State the blood parasite species.
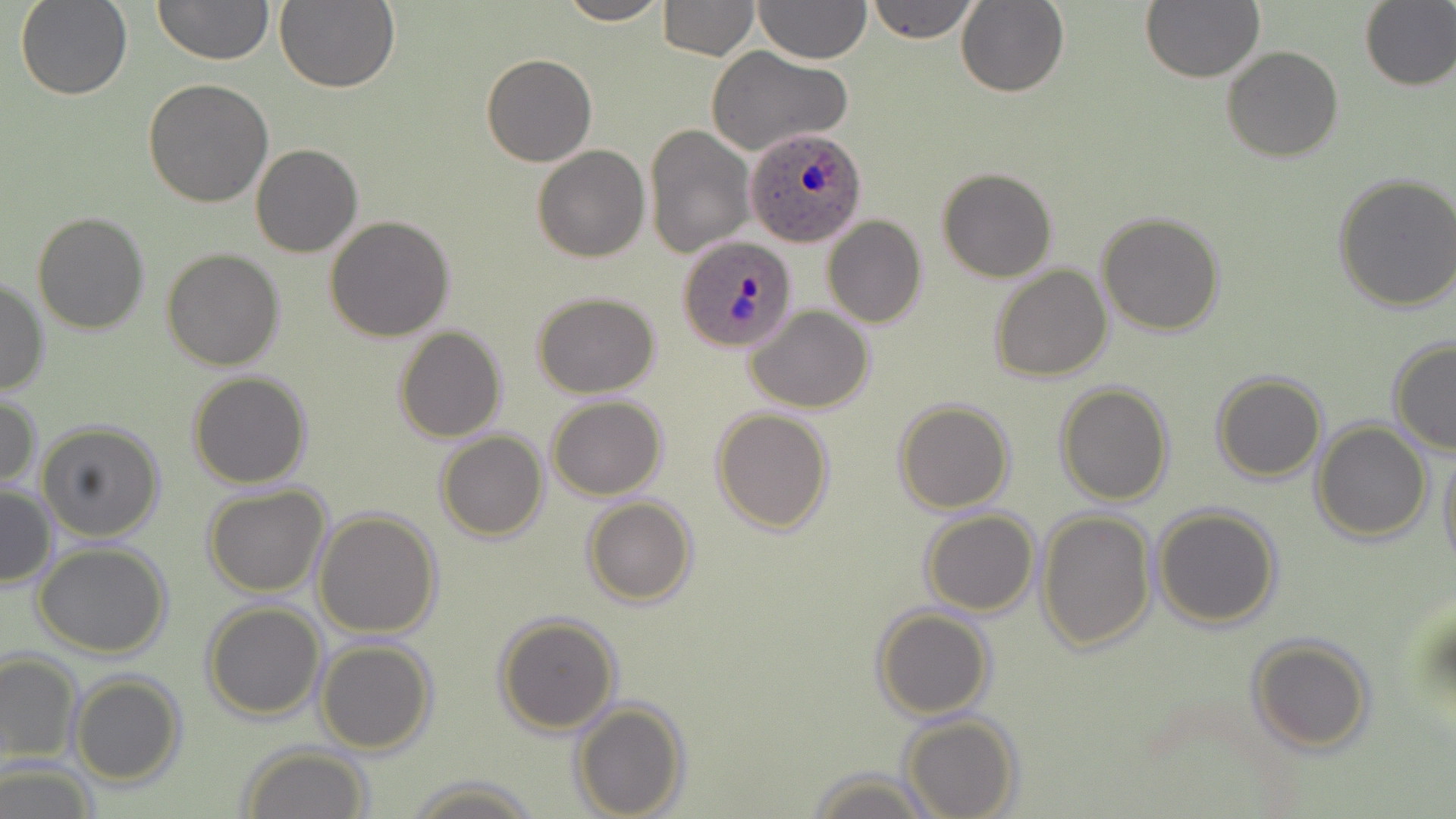

Plasmodium ovale.

Approximate bounding boxes as named x1/y1/x2/y2 corners in pixels. Uninfected red blood cell locations: (x1=16, y1=0, x2=131, y2=100), (x1=153, y1=0, x2=273, y2=67), (x1=275, y1=0, x2=401, y2=95), (x1=555, y1=0, x2=671, y2=25), (x1=657, y1=0, x2=759, y2=59), (x1=753, y1=0, x2=871, y2=65), (x1=866, y1=0, x2=980, y2=43), (x1=1141, y1=0, x2=1264, y2=83), (x1=957, y1=1, x2=1070, y2=97), (x1=1359, y1=1, x2=1456, y2=91), (x1=1222, y1=46, x2=1344, y2=163), (x1=706, y1=47, x2=851, y2=157), (x1=481, y1=53, x2=597, y2=167), (x1=143, y1=79, x2=274, y2=207), (x1=644, y1=122, x2=756, y2=258), (x1=250, y1=144, x2=362, y2=258), (x1=532, y1=146, x2=650, y2=262), (x1=936, y1=167, x2=1058, y2=282), (x1=1333, y1=171, x2=1456, y2=312), (x1=31, y1=210, x2=152, y2=335), (x1=1095, y1=212, x2=1225, y2=336), (x1=324, y1=215, x2=455, y2=341), (x1=824, y1=216, x2=927, y2=329), (x1=162, y1=247, x2=285, y2=370), (x1=171, y1=250, x2=295, y2=489), (x1=990, y1=265, x2=1112, y2=382), (x1=0, y1=276, x2=49, y2=397), (x1=532, y1=291, x2=660, y2=398), (x1=746, y1=306, x2=875, y2=414), (x1=392, y1=325, x2=507, y2=442), (x1=1387, y1=338, x2=1456, y2=455), (x1=188, y1=371, x2=312, y2=488), (x1=1212, y1=371, x2=1326, y2=482), (x1=1054, y1=382, x2=1175, y2=505), (x1=0, y1=394, x2=40, y2=492), (x1=547, y1=396, x2=667, y2=500), (x1=894, y1=399, x2=1015, y2=515), (x1=711, y1=407, x2=834, y2=533), (x1=36, y1=420, x2=165, y2=542), (x1=1311, y1=420, x2=1433, y2=543), (x1=435, y1=430, x2=549, y2=541), (x1=1438, y1=440, x2=1456, y2=573), (x1=1, y1=483, x2=57, y2=589), (x1=204, y1=485, x2=331, y2=597), (x1=582, y1=497, x2=699, y2=606), (x1=1152, y1=504, x2=1282, y2=629), (x1=313, y1=509, x2=442, y2=638), (x1=1037, y1=509, x2=1156, y2=652), (x1=920, y1=510, x2=1039, y2=616), (x1=33, y1=543, x2=172, y2=658), (x1=202, y1=600, x2=327, y2=720), (x1=872, y1=606, x2=992, y2=720), (x1=493, y1=612, x2=622, y2=735), (x1=1247, y1=636, x2=1375, y2=754), (x1=314, y1=639, x2=437, y2=754), (x1=0, y1=650, x2=82, y2=765), (x1=70, y1=674, x2=186, y2=786), (x1=571, y1=698, x2=688, y2=818), (x1=899, y1=713, x2=1021, y2=819), (x1=239, y1=745, x2=373, y2=819), (x1=0, y1=761, x2=99, y2=818), (x1=809, y1=768, x2=936, y2=819), (x1=403, y1=774, x2=543, y2=817). Plasmodium ovale-infected red blood cell locations: (x1=745, y1=125, x2=867, y2=248), (x1=678, y1=234, x2=797, y2=353). Thin blood smear. May-Grünwald-Giemsa stain. Single field of view. Image is 1456×819 pixels. 1000x magnification. Light microscopy.